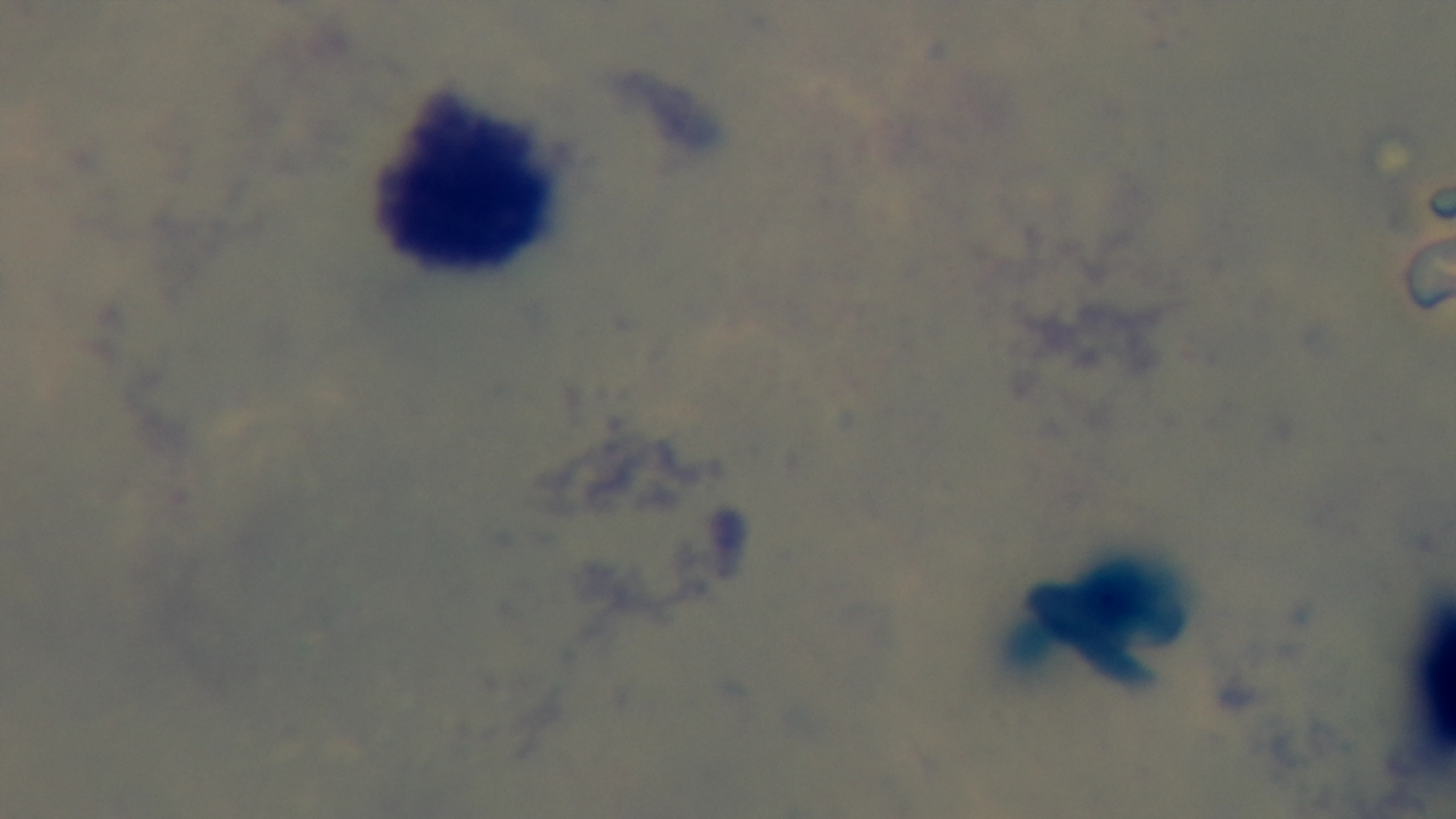

Summary:
  - Field of view: single
  - Stain: Giemsa
  - Capture: mounted 4K digital camera
  - Malaria status: negative
  - Objective: 100x oil immersion
  - Preparation: thick
  - Modality: light microscopy